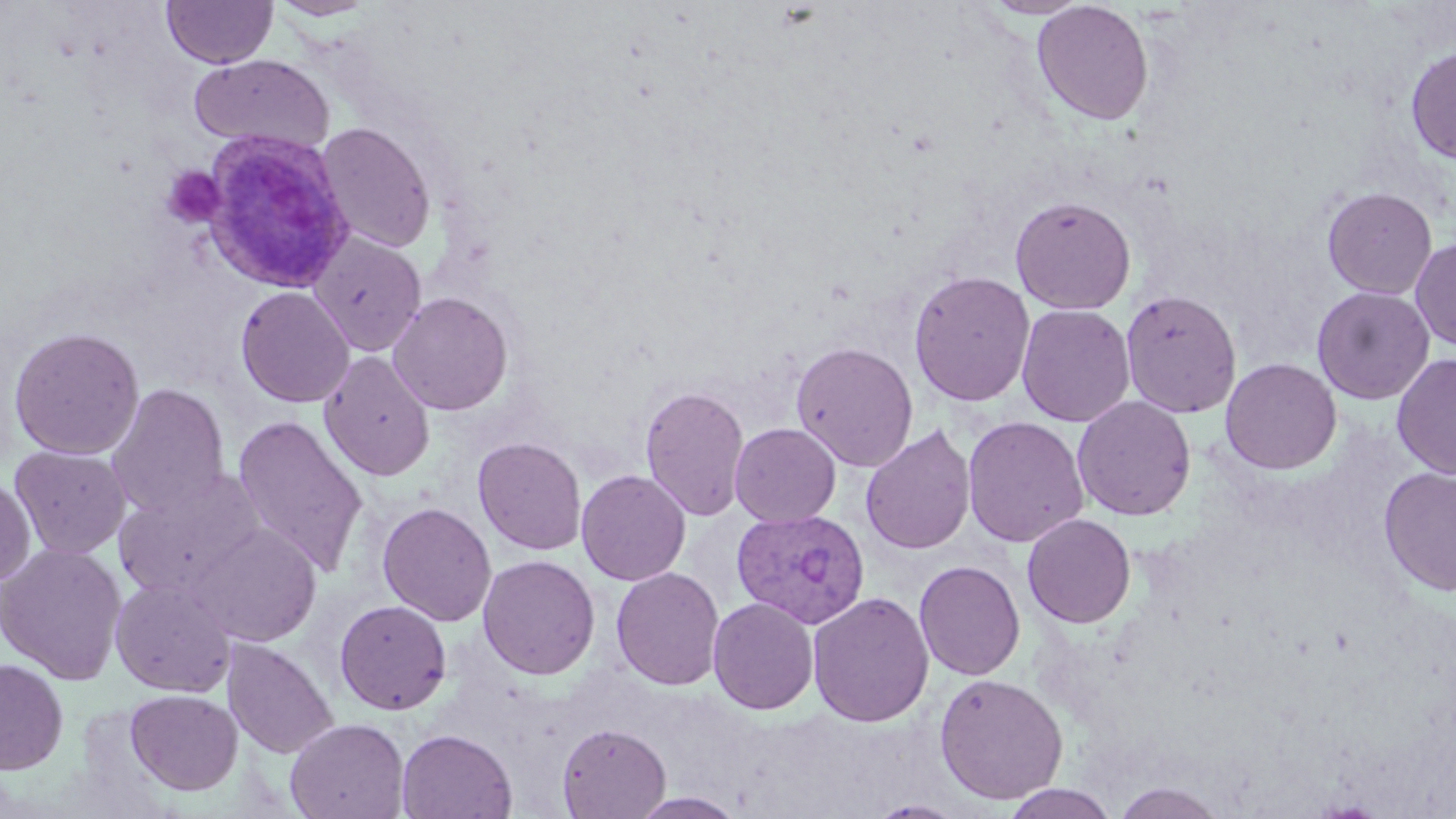

Approximate bounding boxes as [x1, y1, x2, y2] in pixels. Platelet locations: [160, 166, 226, 229]. Plasmodium vivax-infected red blood cell locations: [200, 130, 356, 294], [732, 509, 871, 629]. Uninfected red blood cell locations: [162, 0, 277, 68], [269, 0, 380, 20], [978, 0, 1093, 19], [1032, 1, 1154, 125], [1405, 45, 1456, 164], [190, 54, 335, 153], [315, 122, 436, 254], [1322, 187, 1437, 300], [1010, 195, 1136, 314], [307, 231, 427, 356], [1410, 237, 1456, 352], [908, 270, 1035, 407], [235, 286, 355, 408], [1311, 286, 1434, 404], [1120, 289, 1242, 418], [387, 292, 514, 415], [1016, 303, 1135, 427], [8, 326, 145, 460], [791, 341, 919, 472], [318, 351, 436, 481], [1392, 353, 1456, 481], [1220, 357, 1342, 474], [105, 383, 230, 519], [640, 383, 751, 521], [1072, 395, 1196, 521], [231, 414, 368, 575], [962, 416, 1089, 548], [730, 422, 841, 527], [860, 425, 976, 556], [473, 436, 587, 555], [9, 445, 131, 560], [1379, 466, 1456, 596], [113, 469, 266, 600], [576, 469, 690, 586], [0, 478, 36, 586], [376, 502, 496, 627], [1022, 514, 1136, 628], [189, 523, 322, 646], [0, 542, 127, 684], [477, 555, 600, 679], [914, 560, 1025, 681], [610, 567, 725, 691], [110, 577, 236, 697], [807, 592, 934, 728], [708, 597, 819, 715], [334, 599, 453, 715], [222, 639, 339, 759], [0, 658, 68, 774], [934, 672, 1069, 805], [125, 688, 243, 795], [285, 717, 409, 819], [557, 723, 670, 818], [396, 728, 518, 819], [1112, 782, 1228, 818], [1000, 784, 1120, 818], [629, 791, 747, 818], [867, 799, 970, 818]. Slide-level diagnosis: Plasmodium vivax. Single field of view. Thin blood film. May-Grünwald-Giemsa stain. Image is 1456×819 pixels. Optical microscopy. 1000x magnification.